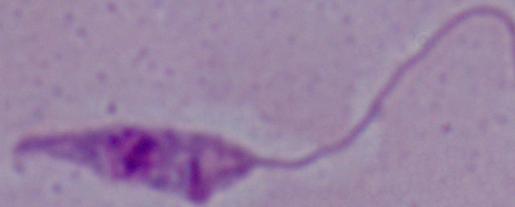

A Leishmania parasite is shown. Photomicrograph. Captured at 1000x magnification.